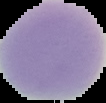

{
  "image_size": "106×103 pixels",
  "image_type": "segmented cell region with the area outside set to black",
  "result": "no malaria parasites detected",
  "preparation": "thin blood film"
}